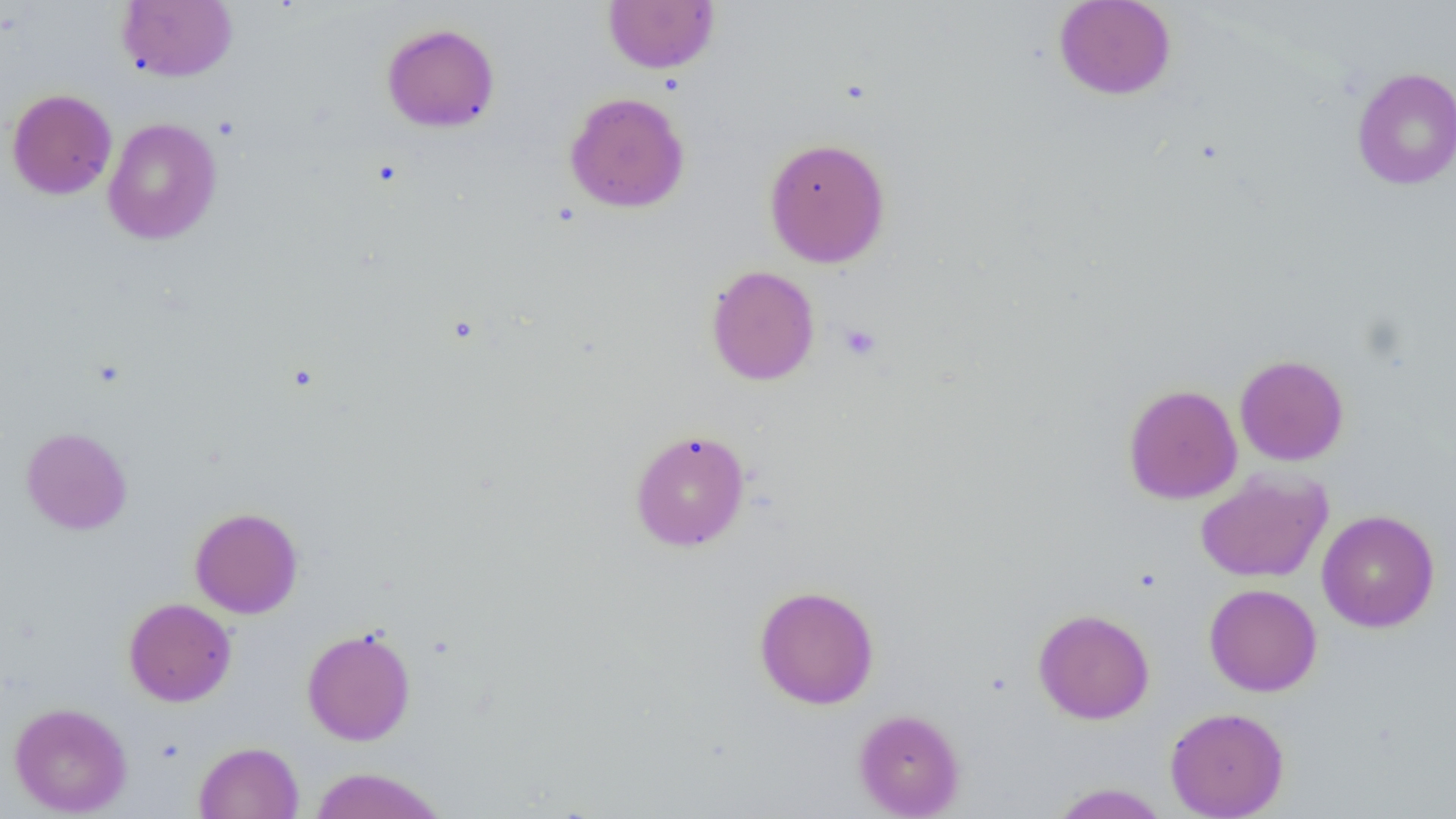
Summary:
  - Coordinate format: approximate bounding boxes as named x1/y1/x2/y2 corners in pixels
  - Platelet locations: (x1=839, y1=323, x2=882, y2=360)
  - Uninfected red blood cell locations: (x1=118, y1=0, x2=238, y2=82), (x1=603, y1=0, x2=719, y2=74), (x1=1053, y1=0, x2=1177, y2=100), (x1=381, y1=23, x2=500, y2=133), (x1=1352, y1=67, x2=1456, y2=190), (x1=6, y1=88, x2=117, y2=199), (x1=564, y1=92, x2=689, y2=213), (x1=102, y1=117, x2=222, y2=245), (x1=763, y1=136, x2=891, y2=268), (x1=705, y1=265, x2=820, y2=386), (x1=1234, y1=354, x2=1349, y2=466), (x1=1123, y1=384, x2=1242, y2=504), (x1=21, y1=427, x2=132, y2=535), (x1=629, y1=428, x2=750, y2=552), (x1=1195, y1=470, x2=1332, y2=583), (x1=189, y1=507, x2=303, y2=619), (x1=1317, y1=510, x2=1440, y2=632), (x1=1204, y1=583, x2=1322, y2=697), (x1=754, y1=585, x2=880, y2=709), (x1=123, y1=598, x2=236, y2=707), (x1=1033, y1=608, x2=1155, y2=724), (x1=301, y1=626, x2=416, y2=746), (x1=9, y1=702, x2=132, y2=817), (x1=1165, y1=706, x2=1289, y2=819), (x1=854, y1=709, x2=965, y2=818), (x1=194, y1=741, x2=304, y2=819), (x1=308, y1=766, x2=448, y2=819), (x1=1049, y1=783, x2=1169, y2=818)
  - Slide-level diagnosis: negative for blood parasites
  - Magnification: 1000x
  - Image size: 1456×819 pixels
  - Modality: light microscopy
  - Preparation: thin blood smear
  - Field of view: one of a larger specimen